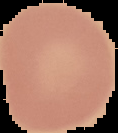
Summary:
  - Image type: cell region segmented out of the field of view; surrounding area masked to black
  - Image size: 118×133 pixels
  - Result: no malaria parasites seen
  - Preparation: thin blood film